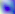

identification: Toxoplasma gondii
magnification: 400x
modality: photomicrograph